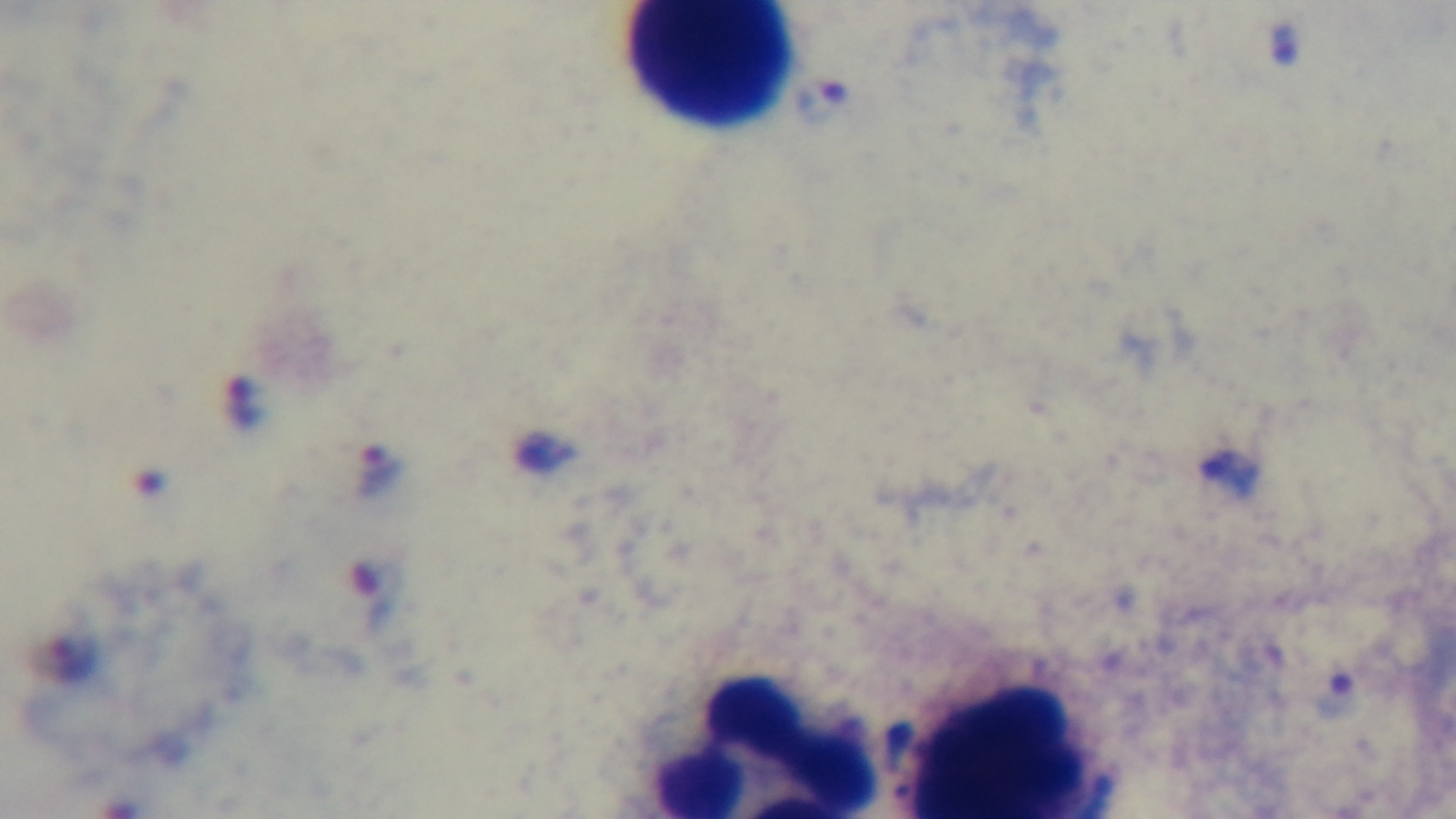

Summary:
  - Modality: light microscopy
  - Field of view: single
  - Stain: Giemsa
  - Objective: 100x oil immersion
  - Malaria status: infected
  - Capture: mounted 4K digital camera
  - Preparation: thick